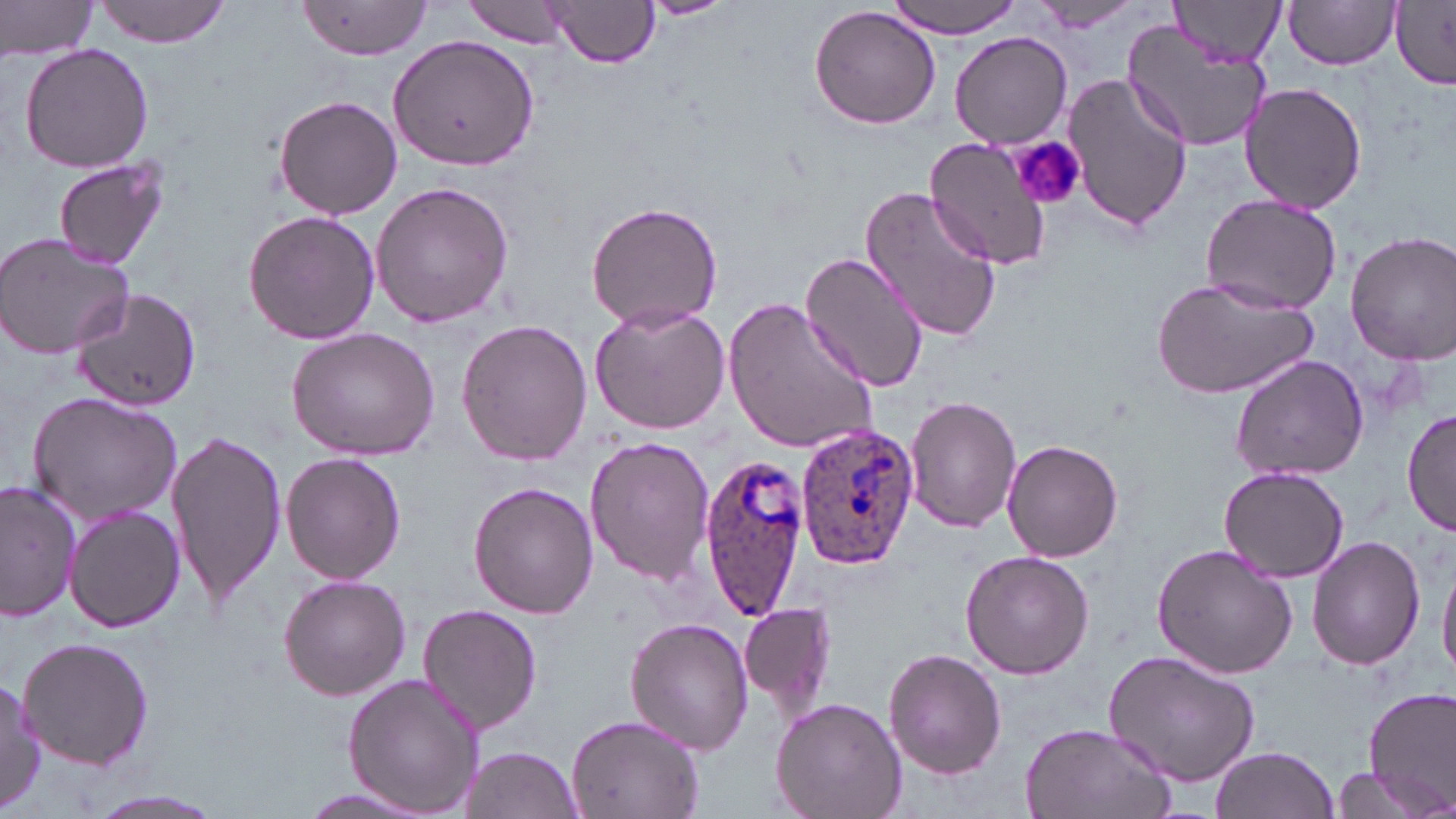

slide_level_diagnosis: Plasmodium ovale
modality: optical microscopy
platelet_locations: 'approximate bounding boxes as [x1, y1, x2, y2] in pixels: [1008, 135, 1087, 213]'
magnification: 1000x
plasmodium_ovale_infected_red_blood_cell_locations: 'approximate bounding boxes as [x1, y1, x2, y2] in pixels: [796, 420, 919, 571], [698, 452, 812, 618]'
stain: May-Grünwald-Giemsa
preparation: thin blood film
uninfected_red_blood_cell_locations: 'approximate bounding boxes as [x1, y1, x2, y2] in pixels: [0, 0, 101, 60], [94, 0, 231, 46], [638, 0, 734, 19], [892, 0, 1022, 37], [1172, 0, 1285, 68], [462, 1, 572, 48], [1028, 1, 1144, 33], [1282, 1, 1401, 71], [296, 2, 433, 59], [545, 2, 659, 69], [1391, 4, 1455, 87], [810, 7, 941, 130], [1122, 20, 1270, 154], [388, 32, 539, 173], [950, 32, 1072, 149], [19, 42, 155, 174], [1063, 74, 1192, 234], [1238, 80, 1367, 214], [272, 94, 403, 220], [924, 136, 1054, 270], [53, 157, 170, 271], [369, 180, 516, 329], [860, 185, 1002, 343], [1198, 192, 1344, 314], [586, 200, 724, 331], [243, 208, 380, 347], [1345, 231, 1456, 363], [0, 232, 135, 360], [800, 248, 930, 394], [1150, 277, 1317, 402], [69, 288, 203, 409], [725, 295, 881, 458], [590, 300, 733, 435], [455, 317, 592, 465], [284, 326, 442, 461], [1230, 353, 1370, 483], [26, 390, 183, 526], [905, 395, 1022, 533], [1403, 408, 1455, 540], [166, 427, 287, 610], [584, 434, 714, 588], [1001, 439, 1124, 562], [281, 452, 406, 585], [1218, 466, 1350, 583], [0, 481, 79, 621], [469, 481, 599, 618], [1173, 487, 1322, 645], [66, 504, 185, 633], [1309, 535, 1426, 669], [1152, 542, 1299, 679], [960, 550, 1095, 680], [1438, 556, 1456, 684], [277, 573, 411, 701], [740, 600, 837, 716], [416, 603, 544, 734], [626, 616, 753, 755], [17, 635, 155, 770], [884, 648, 1006, 778], [1103, 650, 1261, 787], [342, 674, 486, 815], [0, 678, 44, 815], [1363, 689, 1456, 810], [770, 696, 908, 819], [566, 712, 705, 819], [1020, 721, 1175, 819], [1210, 746, 1340, 819], [461, 747, 584, 817], [1326, 765, 1440, 819], [294, 786, 433, 816], [76, 787, 232, 819]'
image_size: 1456×819 pixels
field_of_view: one of a larger specimen